Evaluate for Plasmodium parasites.
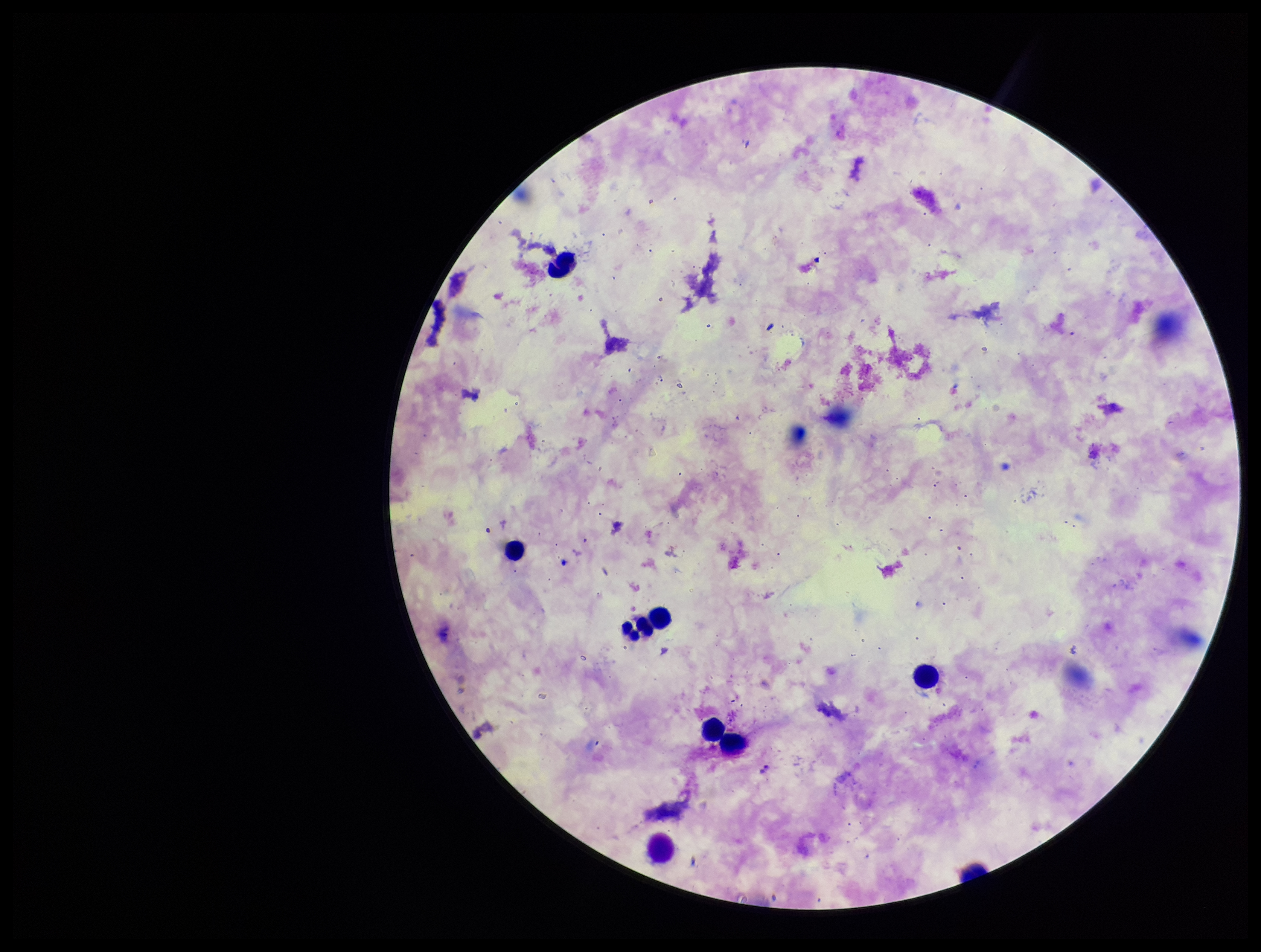

None detected.

Giemsa stain. One field from this slide. Leukocyte count: 8. Patient malaria status: infected. Parasite count: 0. Species reported for this patient: Plasmodium falciparum. Preparation: thick smear. Image is 1261×952 pixels. Photographed through the microscope eyepiece with a smartphone camera.